Report the malaria status of this cell.
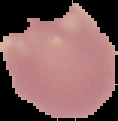
It is uninfected.

Summary:
  - Preparation: thin blood smear
  - Image size: 118×121 pixels
  - Image type: segmented cell region on a black background